State the preparation type.
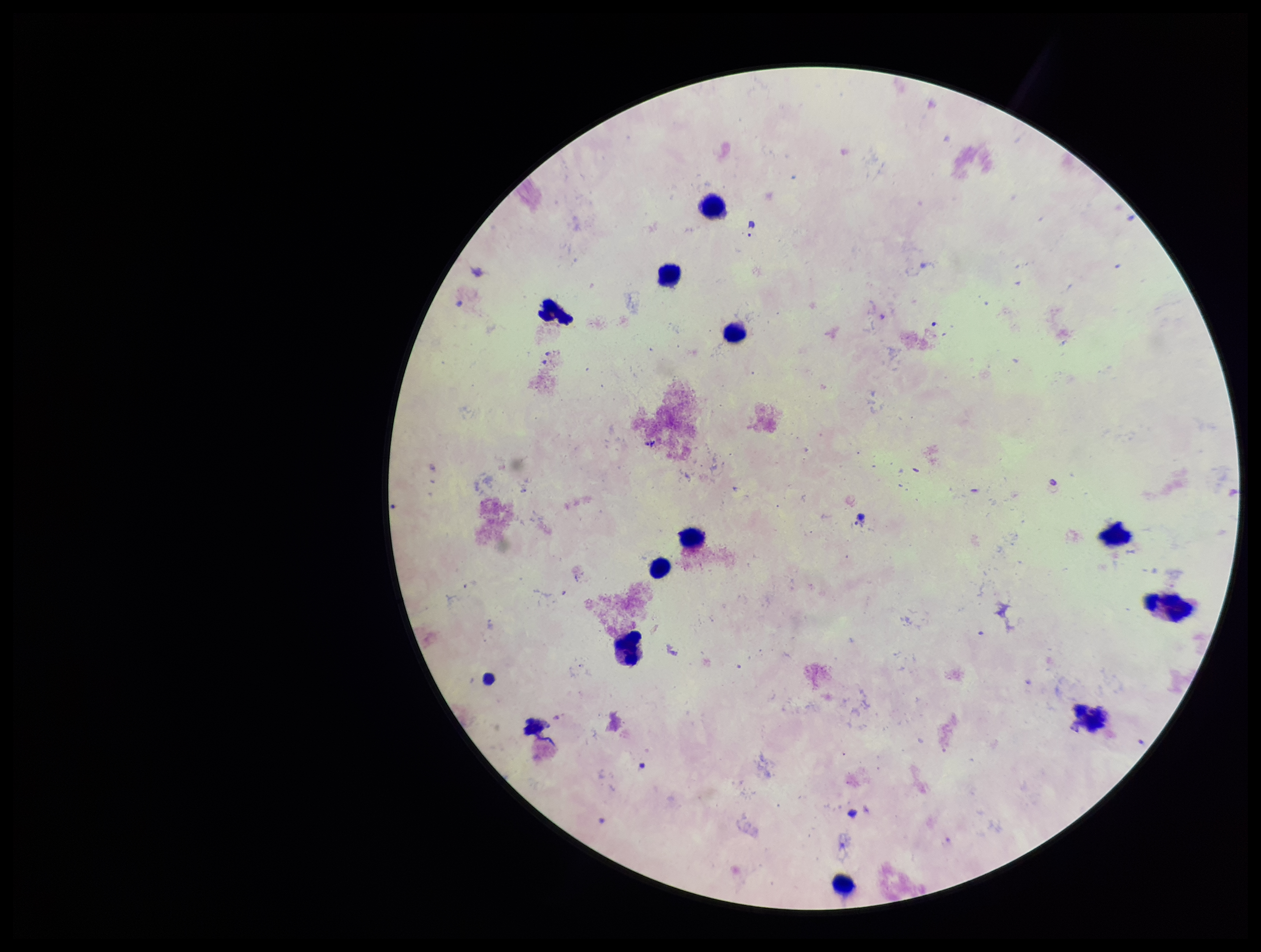
A thick smear.

Patient malaria status: negative. Plasmodium parasites: none detected. Smartphone photograph taken through the eyepiece of a microscope. Giemsa stain. Parasite count: 0. Leukocyte count: 11. Single field of view. Image is 1261×952 pixels.